Give the position of every Plasmodium falciparum parasite, noting its life-cycle stage.
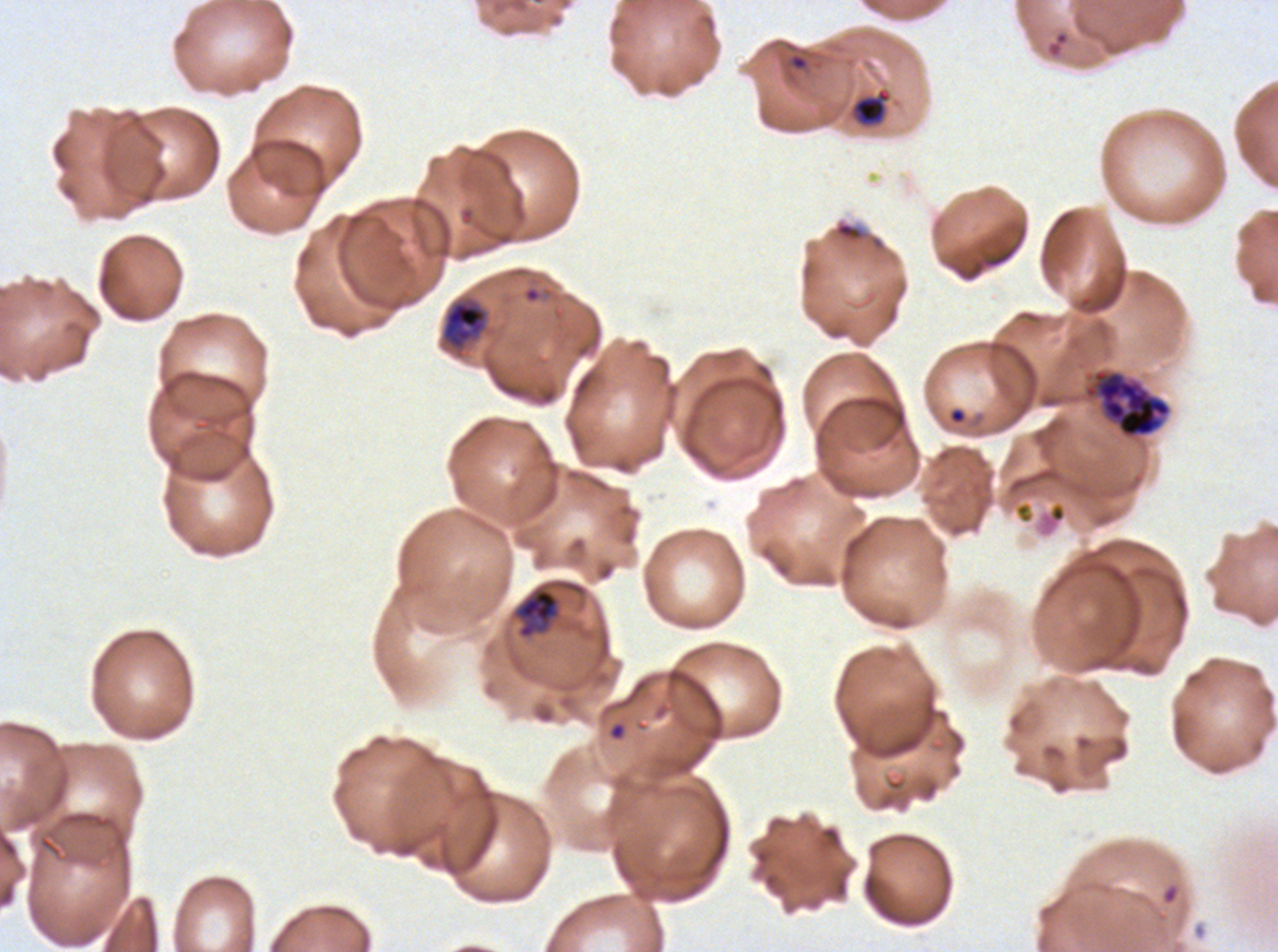
Approximate bounding rectangles given as corner coordinates in pixels from the top-left.
Rings: (x1=608, y1=721, x2=627, y2=741).
Late-ring/early-trophozoite forms: (x1=851, y1=87, x2=891, y2=127), (x1=442, y1=300, x2=487, y2=349), (x1=514, y1=587, x2=560, y2=639).
Early schizonts: (x1=1085, y1=369, x2=1172, y2=438).
No mid trophozoites, late trophozoites, late schizonts, segmenters, or gametocytes observed.

Debris locations: (x1=831, y1=219, x2=887, y2=253). Giemsa-stained preparation. Life-cycle stages observed: ring, late-ring/early-trophozoite, early schizont. Image is 1278×952 pixels. Plasmodium falciparum from a patient in The Gambia, cultured ex vivo for 24 to 48 hours. Thin blood film. A sub-image separated from a larger composite.